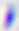 Micrograph. 400x magnification. Toxoplasma gondii is seen.